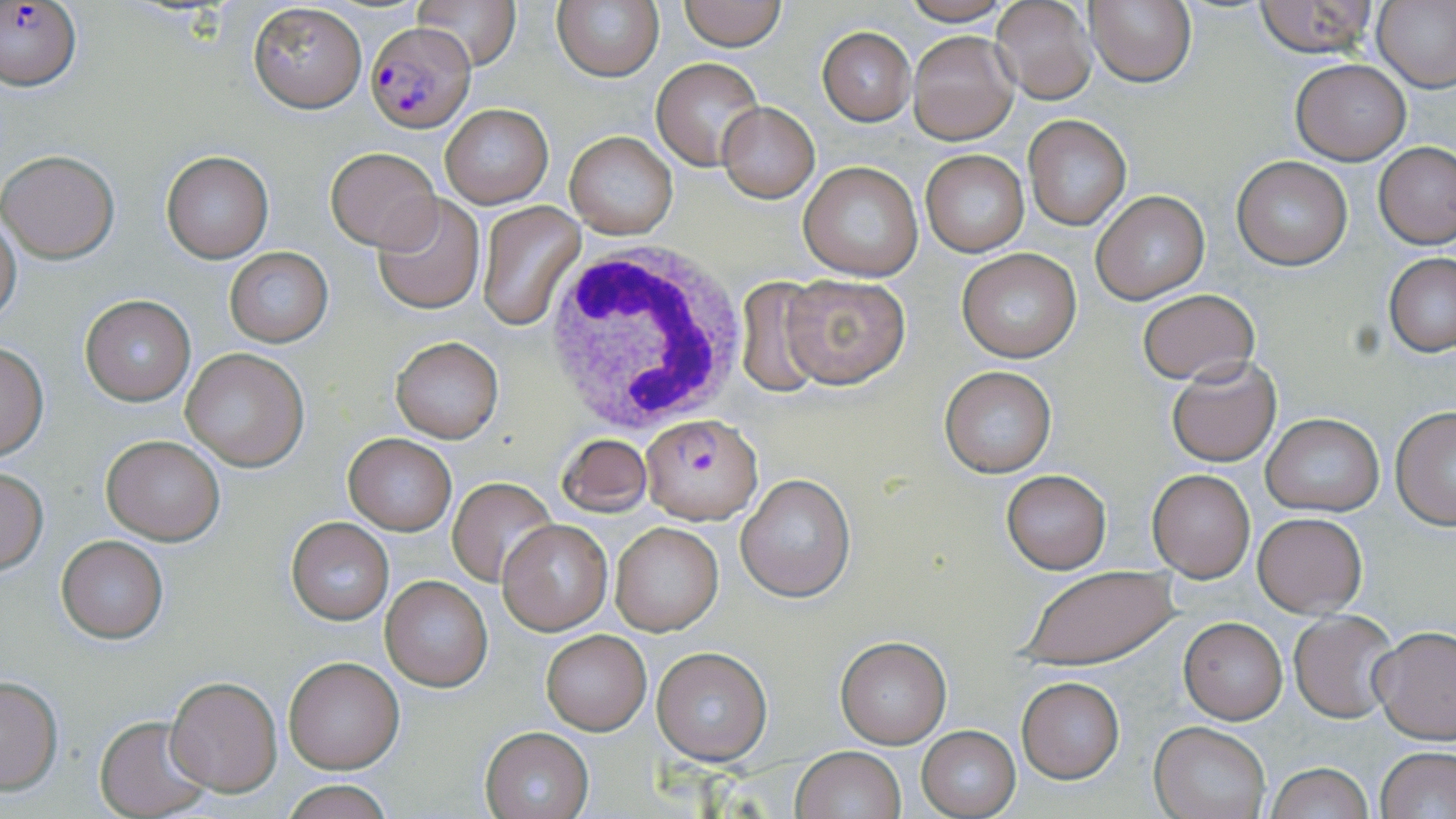

Approximate bounding boxes as (x1, y1, x2, y2) in pixels. Uninfected red blood cell locations: (408, 0, 521, 71), (551, 0, 666, 83), (678, 0, 787, 50), (1085, 0, 1197, 88), (1255, 0, 1379, 57), (897, 1, 1014, 26), (1373, 1, 1456, 93), (248, 2, 367, 113), (992, 2, 1096, 105), (817, 28, 915, 125), (908, 30, 1018, 144), (651, 58, 764, 168), (1291, 59, 1410, 165), (440, 103, 553, 208), (718, 103, 818, 202), (1024, 116, 1131, 231), (564, 132, 679, 241), (1375, 141, 1455, 249), (326, 146, 441, 252), (920, 148, 1030, 258), (0, 149, 120, 262), (161, 150, 273, 261), (1231, 157, 1353, 271), (798, 162, 926, 282), (1091, 191, 1209, 303), (372, 193, 486, 314), (477, 201, 584, 329), (0, 214, 21, 326), (957, 248, 1082, 364), (224, 249, 333, 347), (1385, 253, 1456, 358), (782, 273, 911, 388), (733, 277, 830, 394), (1136, 290, 1259, 385), (80, 294, 195, 405), (389, 336, 504, 443), (0, 342, 48, 461), (180, 348, 309, 471), (1165, 356, 1282, 466), (938, 364, 1058, 478), (1391, 408, 1456, 528), (1260, 413, 1385, 516), (558, 433, 651, 517), (102, 434, 226, 544), (344, 434, 456, 534), (0, 468, 49, 573), (1147, 468, 1256, 581), (1001, 470, 1111, 574), (736, 474, 855, 602), (447, 477, 556, 586), (1253, 512, 1367, 618), (286, 517, 394, 624), (498, 520, 612, 633), (608, 521, 723, 636), (57, 535, 168, 643), (1020, 566, 1179, 671), (380, 575, 492, 691), (1290, 612, 1398, 721), (1179, 618, 1287, 723), (1370, 625, 1456, 744), (540, 629, 651, 735), (835, 638, 951, 748), (652, 647, 772, 765), (282, 656, 404, 773), (165, 675, 283, 794), (0, 676, 63, 793), (1016, 676, 1124, 783), (95, 713, 214, 818), (1149, 720, 1271, 819), (918, 726, 1020, 817), (480, 728, 593, 818), (793, 746, 905, 819), (1377, 748, 1456, 819), (1264, 762, 1374, 819), (277, 782, 395, 817). White blood cell locations: (541, 239, 750, 435). Plasmodium falciparum-infected red blood cell locations: (4, 1, 80, 89), (366, 21, 473, 133), (640, 413, 762, 525). Slide-level diagnosis: Plasmodium falciparum. Optical microscopy. Thin blood smear. Captured at 1000x magnification. Single field of view. May-Grünwald-Giemsa-stained preparation. Image is 1456×819 pixels.